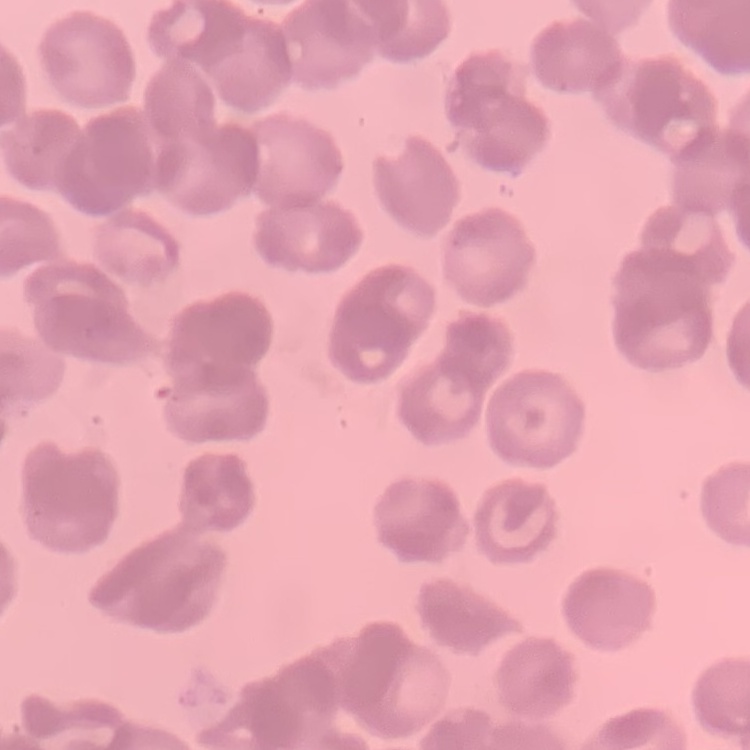
The erythrocytes exhibit rouleaux formation. Thin blood film. Field's or Giemsa stain. Square crop of a larger photomicrograph.